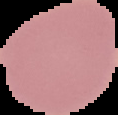
Segmented cell region on a black background. Malaria status: uninfected. Image is 118×115 pixels. From a thin blood smear.